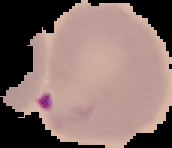

preparation = thin blood film
image type = segmented cell region on a black background
malaria status = parasitized
image size = 172×148 pixels